Outline each Plasmodium falciparum-infected red blood cell.
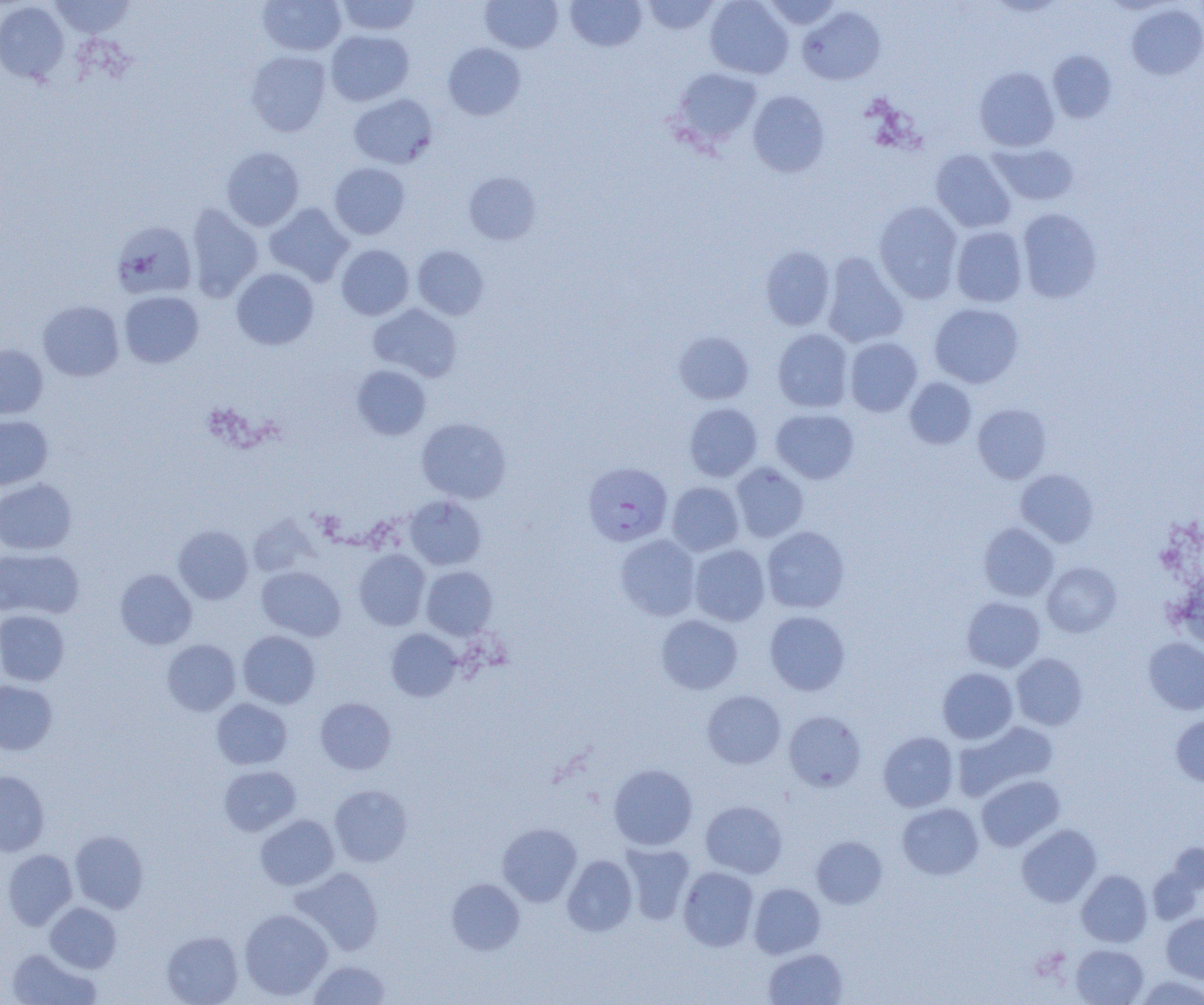
Approximate bounding boxes as (x1,y1)-(x2,y2) corner pairs in pixels.
Plasmodium falciparum-infected red blood cells: (583,463)-(673,546).

Summary:
  - Uninfected red blood cell locations: (51,0)-(135,38), (336,0)-(421,35), (480,0)-(562,53), (566,0)-(646,51), (642,0)-(720,35), (705,0)-(793,78), (763,0)-(841,30), (0,1)-(69,84), (258,1)-(346,56), (1126,4)-(1204,80), (798,6)-(885,86), (325,29)-(414,106), (443,43)-(525,120), (245,50)-(331,136), (1048,50)-(1117,122), (975,67)-(1059,152), (672,68)-(761,146), (748,90)-(830,177), (348,94)-(438,169), (989,142)-(1080,206), (221,146)-(305,230), (930,149)-(1016,233), (329,162)-(410,239), (463,172)-(542,244), (874,201)-(963,303), (265,202)-(354,286), (185,203)-(263,302), (1017,208)-(1103,303), (111,221)-(198,299), (951,226)-(1028,307), (336,244)-(414,320), (412,245)-(489,320), (760,246)-(836,330), (822,253)-(908,348), (231,267)-(319,350), (119,290)-(204,368), (38,300)-(124,381), (368,303)-(462,382), (929,303)-(1024,388), (772,329)-(853,412), (673,331)-(754,404), (845,337)-(922,416), (0,344)-(48,418), (351,364)-(431,440), (905,378)-(976,449), (685,403)-(762,481), (973,404)-(1052,483), (771,409)-(859,483), (0,416)-(53,490), (416,417)-(511,503), (731,463)-(809,542), (1016,469)-(1099,547), (0,479)-(77,554), (667,481)-(744,556), (404,495)-(487,570), (248,515)-(319,578), (979,522)-(1059,601), (173,525)-(253,604), (762,526)-(850,613), (614,534)-(701,620), (689,544)-(770,626), (0,548)-(83,620), (353,549)-(430,630), (1042,561)-(1121,637), (257,566)-(346,641), (421,566)-(497,639), (115,569)-(197,649), (1172,570)-(1204,651), (962,596)-(1045,672), (0,610)-(69,686), (764,610)-(850,695), (656,615)-(742,694), (386,629)-(461,701), (238,630)-(321,709), (1143,637)-(1204,714), (161,639)-(241,716), (1012,653)-(1087,730), (937,667)-(1018,744), (0,681)-(57,754), (702,690)-(786,768), (316,697)-(396,774), (212,698)-(292,769), (783,710)-(866,792), (1170,715)-(1204,787), (953,721)-(1058,802), (878,731)-(959,812), (608,764)-(697,850), (219,766)-(301,836), (0,770)-(49,855), (976,775)-(1064,851), (329,785)-(412,867), (700,800)-(787,879), (897,803)-(983,880), (255,814)-(339,890), (498,823)-(582,906), (1017,824)-(1101,907), (70,830)-(149,913), (811,836)-(887,909), (620,842)-(695,925), (1168,842)-(1204,894), (2,849)-(77,929), (562,855)-(637,936), (290,866)-(384,955), (678,866)-(759,951), (1147,866)-(1202,925), (1076,870)-(1152,947), (446,878)-(525,955), (748,883)-(825,958), (45,902)-(122,973), (239,908)-(333,1001), (1161,912)-(1204,983), (162,931)-(243,1005), (1071,944)-(1148,1004), (7,948)-(100,1005), (764,948)-(847,1005), (308,959)-(392,1004), (1136,976)-(1204,1004)
  - Slide-level diagnosis: Plasmodium falciparum
  - Image size: 1204×1005 pixels
  - Magnification: 1000x
  - Modality: light microscopy
  - Preparation: thin blood smear
  - Field of view: one of a larger specimen